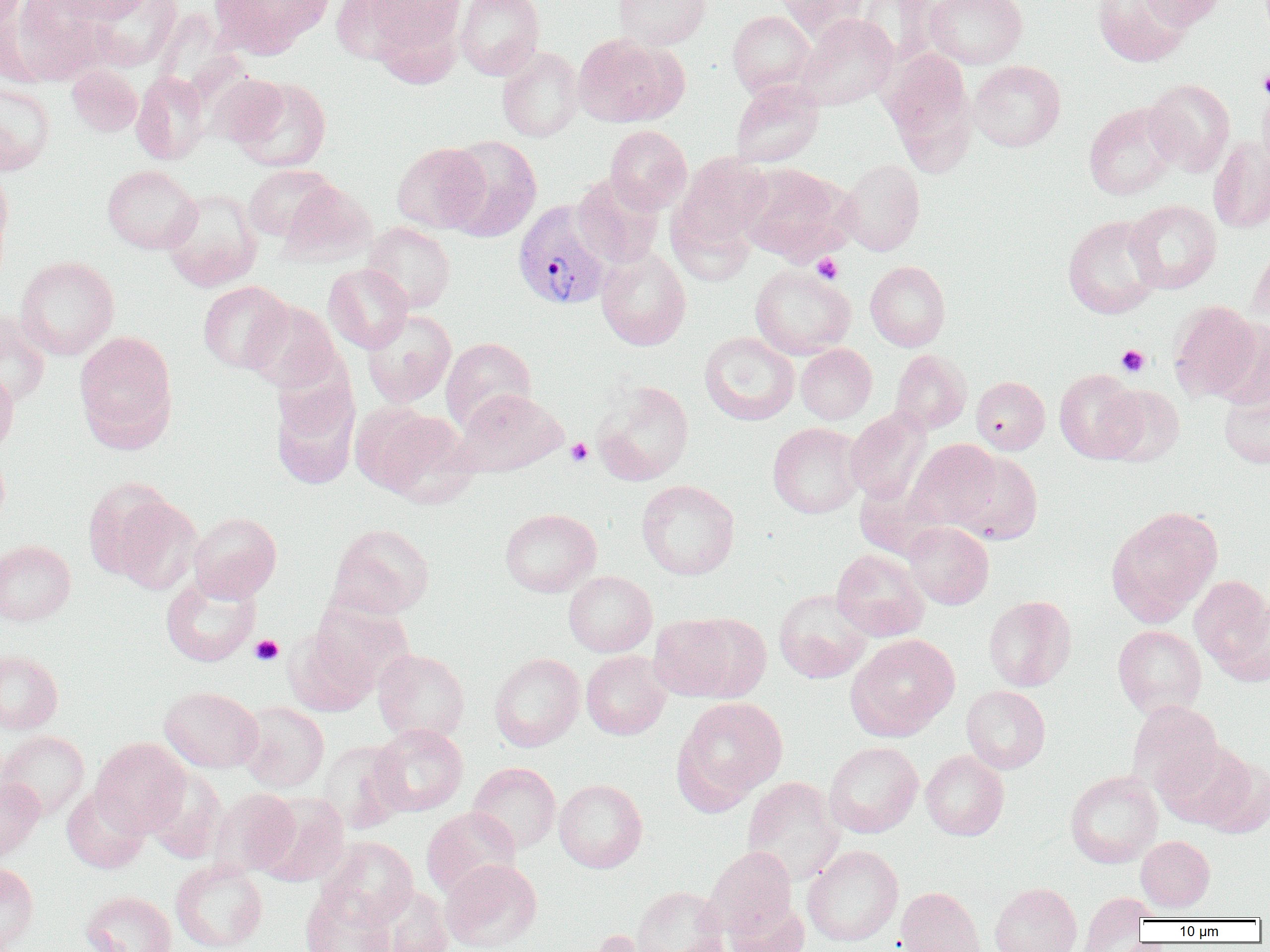 Approximate bounding boxes as named x1/y1/x2/y2 corners in pixels. Platelet locations: (x1=1258, y1=68, x2=1270, y2=96), (x1=812, y1=253, x2=843, y2=284), (x1=1116, y1=345, x2=1149, y2=377), (x1=566, y1=438, x2=593, y2=466), (x1=250, y1=634, x2=284, y2=665). Plasmodium vivax-infected red blood cell locations: (x1=513, y1=199, x2=613, y2=310). Uninfected red blood cell locations: (x1=4, y1=0, x2=108, y2=86), (x1=53, y1=0, x2=155, y2=23), (x1=82, y1=0, x2=183, y2=72), (x1=208, y1=0, x2=334, y2=58), (x1=350, y1=0, x2=464, y2=64), (x1=455, y1=0, x2=544, y2=80), (x1=614, y1=0, x2=710, y2=49), (x1=776, y1=0, x2=871, y2=41), (x1=856, y1=0, x2=940, y2=69), (x1=925, y1=0, x2=1027, y2=69), (x1=1092, y1=0, x2=1193, y2=67), (x1=1138, y1=0, x2=1228, y2=28), (x1=727, y1=10, x2=815, y2=98), (x1=795, y1=14, x2=898, y2=111), (x1=573, y1=33, x2=686, y2=127), (x1=497, y1=47, x2=584, y2=142), (x1=882, y1=48, x2=977, y2=171), (x1=969, y1=60, x2=1066, y2=152), (x1=66, y1=65, x2=142, y2=136), (x1=131, y1=71, x2=211, y2=165), (x1=206, y1=72, x2=289, y2=147), (x1=230, y1=76, x2=332, y2=172), (x1=1144, y1=78, x2=1236, y2=175), (x1=730, y1=79, x2=824, y2=167), (x1=0, y1=80, x2=55, y2=176), (x1=1258, y1=85, x2=1270, y2=177), (x1=1083, y1=103, x2=1180, y2=200), (x1=605, y1=125, x2=692, y2=213), (x1=442, y1=135, x2=542, y2=242), (x1=1208, y1=136, x2=1270, y2=233), (x1=391, y1=142, x2=489, y2=233), (x1=673, y1=153, x2=773, y2=249), (x1=839, y1=159, x2=925, y2=255), (x1=739, y1=163, x2=852, y2=263), (x1=0, y1=165, x2=14, y2=273), (x1=102, y1=165, x2=201, y2=254), (x1=243, y1=165, x2=338, y2=241), (x1=572, y1=173, x2=664, y2=268), (x1=279, y1=182, x2=377, y2=266), (x1=162, y1=189, x2=263, y2=292), (x1=1125, y1=199, x2=1222, y2=294), (x1=667, y1=204, x2=756, y2=286), (x1=1062, y1=214, x2=1164, y2=319), (x1=362, y1=222, x2=456, y2=313), (x1=596, y1=245, x2=691, y2=351), (x1=1246, y1=245, x2=1270, y2=339), (x1=15, y1=256, x2=119, y2=360), (x1=865, y1=261, x2=950, y2=351), (x1=323, y1=264, x2=413, y2=353), (x1=750, y1=265, x2=855, y2=359), (x1=197, y1=280, x2=293, y2=373), (x1=243, y1=300, x2=342, y2=393), (x1=1169, y1=301, x2=1263, y2=403), (x1=361, y1=309, x2=457, y2=407), (x1=0, y1=311, x2=51, y2=407), (x1=74, y1=330, x2=177, y2=449), (x1=699, y1=332, x2=799, y2=425), (x1=441, y1=337, x2=537, y2=432), (x1=795, y1=343, x2=877, y2=424), (x1=890, y1=349, x2=972, y2=434), (x1=0, y1=364, x2=19, y2=457), (x1=1054, y1=368, x2=1145, y2=463), (x1=270, y1=371, x2=361, y2=491), (x1=971, y1=376, x2=1050, y2=454), (x1=592, y1=379, x2=694, y2=485), (x1=1219, y1=382, x2=1270, y2=469), (x1=1099, y1=384, x2=1185, y2=467), (x1=453, y1=389, x2=568, y2=476), (x1=354, y1=405, x2=474, y2=503), (x1=845, y1=408, x2=932, y2=504), (x1=767, y1=422, x2=865, y2=518), (x1=906, y1=439, x2=1002, y2=531), (x1=0, y1=447, x2=10, y2=534), (x1=953, y1=452, x2=1043, y2=544), (x1=637, y1=479, x2=739, y2=580), (x1=88, y1=483, x2=201, y2=592), (x1=1106, y1=506, x2=1223, y2=625), (x1=500, y1=508, x2=601, y2=597), (x1=188, y1=512, x2=282, y2=603), (x1=903, y1=521, x2=994, y2=609), (x1=328, y1=523, x2=435, y2=620), (x1=0, y1=540, x2=76, y2=625), (x1=831, y1=548, x2=930, y2=641), (x1=564, y1=571, x2=657, y2=656), (x1=161, y1=574, x2=260, y2=667), (x1=1189, y1=576, x2=1270, y2=681), (x1=774, y1=589, x2=872, y2=683), (x1=983, y1=595, x2=1077, y2=691), (x1=310, y1=598, x2=413, y2=691), (x1=648, y1=613, x2=756, y2=702), (x1=1112, y1=625, x2=1206, y2=718), (x1=285, y1=630, x2=377, y2=716), (x1=846, y1=634, x2=959, y2=740), (x1=373, y1=648, x2=470, y2=743), (x1=0, y1=649, x2=63, y2=734), (x1=581, y1=651, x2=671, y2=740), (x1=489, y1=653, x2=585, y2=751), (x1=961, y1=685, x2=1050, y2=774), (x1=159, y1=686, x2=263, y2=773), (x1=673, y1=696, x2=788, y2=809), (x1=1127, y1=700, x2=1223, y2=796), (x1=237, y1=702, x2=329, y2=793), (x1=370, y1=724, x2=468, y2=816), (x1=0, y1=730, x2=90, y2=820), (x1=91, y1=738, x2=190, y2=836), (x1=1155, y1=739, x2=1253, y2=829), (x1=317, y1=740, x2=409, y2=834), (x1=824, y1=741, x2=923, y2=838), (x1=921, y1=750, x2=1009, y2=840), (x1=1200, y1=756, x2=1270, y2=838), (x1=467, y1=762, x2=561, y2=854), (x1=143, y1=768, x2=228, y2=864), (x1=1065, y1=770, x2=1163, y2=868), (x1=0, y1=776, x2=43, y2=864), (x1=742, y1=777, x2=845, y2=885), (x1=554, y1=779, x2=647, y2=873), (x1=61, y1=786, x2=149, y2=874), (x1=208, y1=788, x2=300, y2=878), (x1=255, y1=792, x2=350, y2=887), (x1=421, y1=807, x2=520, y2=899), (x1=1136, y1=835, x2=1215, y2=912), (x1=318, y1=836, x2=418, y2=929), (x1=802, y1=844, x2=903, y2=946), (x1=703, y1=846, x2=797, y2=937), (x1=441, y1=859, x2=542, y2=951), (x1=170, y1=860, x2=268, y2=952), (x1=0, y1=862, x2=39, y2=951), (x1=989, y1=882, x2=1082, y2=952), (x1=373, y1=886, x2=454, y2=952), (x1=631, y1=886, x2=727, y2=952), (x1=895, y1=886, x2=986, y2=952), (x1=300, y1=888, x2=393, y2=952), (x1=80, y1=890, x2=177, y2=952), (x1=1079, y1=892, x2=1153, y2=952), (x1=724, y1=899, x2=809, y2=952), (x1=585, y1=929, x2=675, y2=952). Slide-level diagnosis: Plasmodium vivax. Single field of view. Thin blood smear. Optical microscopy. Captured at 1000x magnification. Image is 1270×952 pixels.